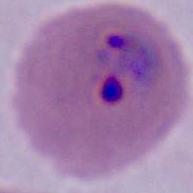

{
  "modality": "photomicrograph",
  "magnification": "400x or 1000x",
  "identification": "Plasmodium"
}